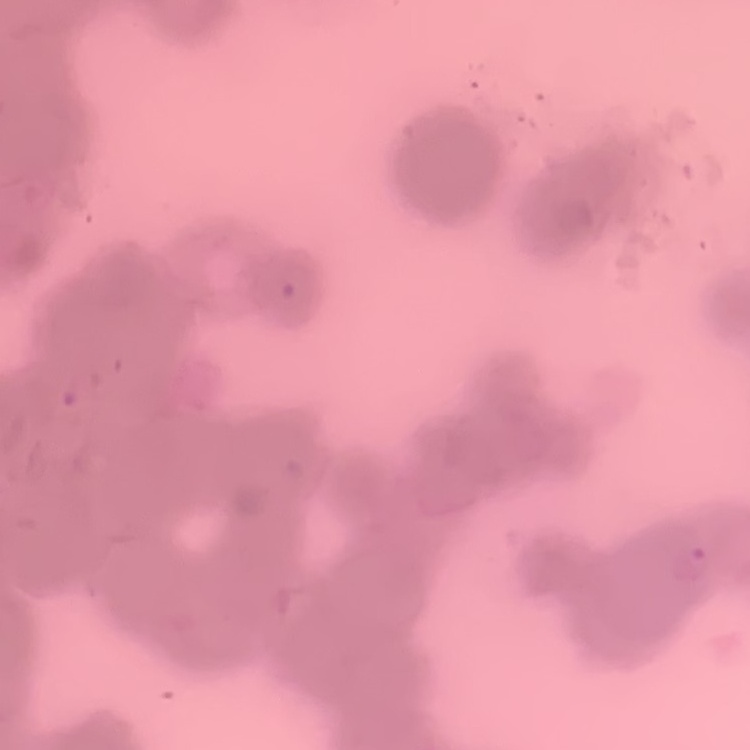

{
  "red_blood_cell_morphology": "rouleaux formation",
  "preparation": "thin blood smear",
  "image_type": "one tile cut from a larger photomicrograph",
  "stain": "Field's or Giemsa"
}